Locate every blood parasite and identify its species.
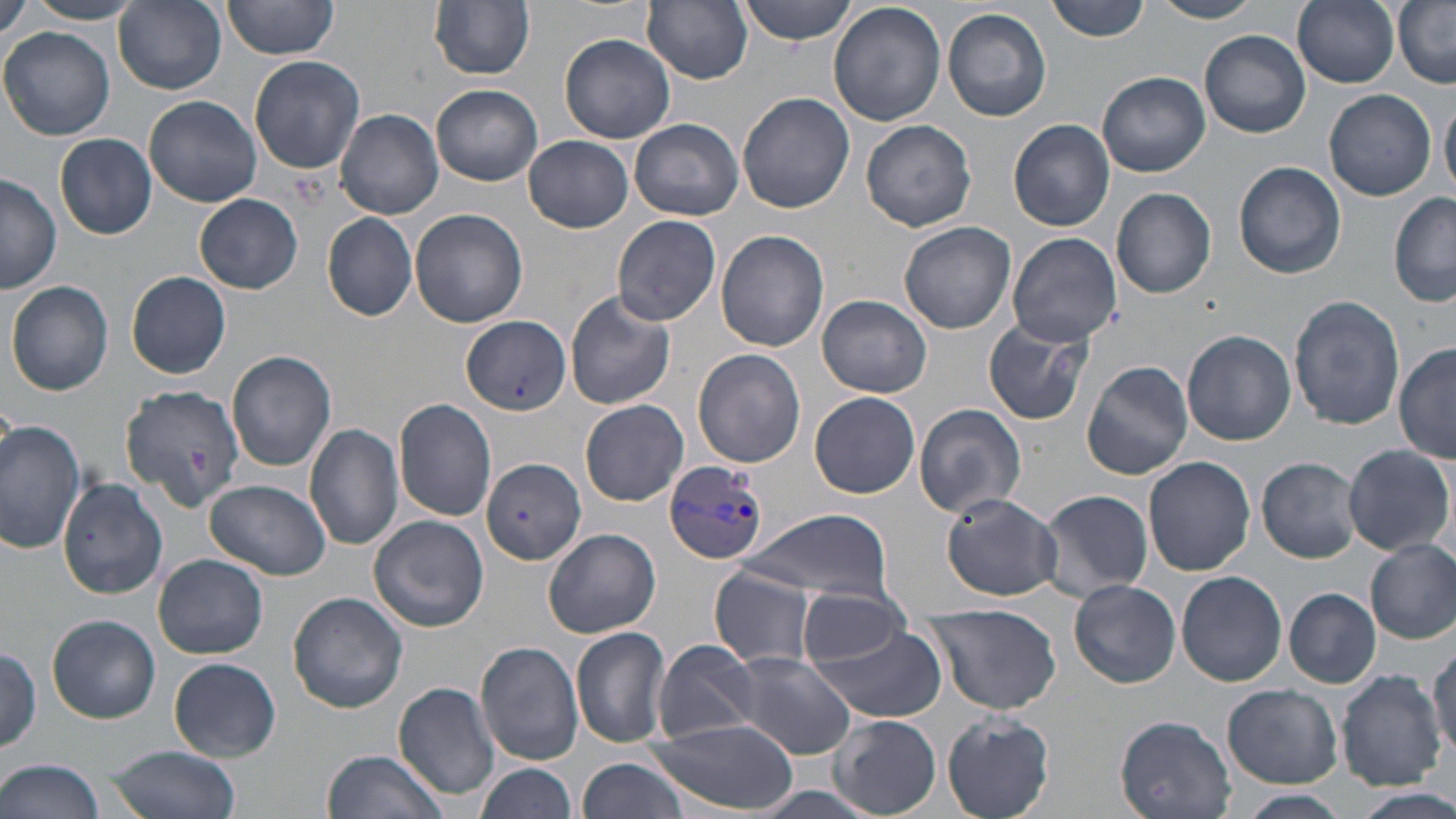

Approximate bounding boxes as (x1,y1)-(x2,y2) corner pairs in pixels.
Plasmodium vivax-infected red blood cells: (661,460)-(769,564).
No Plasmodium falciparum, Plasmodium ovale, Plasmodium malariae, Babesia divergens, or Trypanosoma brucei observed.

Uninfected red blood cell locations: (2,0)-(33,41), (429,0)-(536,80), (643,0)-(753,85), (736,0)-(861,46), (1047,0)-(1152,43), (1150,0)-(1264,23), (1292,0)-(1401,88), (23,1)-(146,24), (114,1)-(227,94), (220,2)-(341,63), (1394,2)-(1456,87), (827,3)-(945,128), (942,8)-(1052,122), (2,27)-(115,140), (1200,30)-(1311,138), (559,33)-(676,144), (249,56)-(365,174), (1099,71)-(1210,177), (431,84)-(543,185), (1323,88)-(1437,201), (737,91)-(854,213), (1440,94)-(1456,200), (144,95)-(262,208), (337,109)-(444,219), (631,118)-(744,221), (1008,119)-(1113,232), (862,120)-(976,233), (54,133)-(157,239), (524,135)-(632,233), (1233,161)-(1347,279), (0,175)-(62,294), (1111,186)-(1218,299), (194,193)-(303,293), (1389,194)-(1455,309), (409,207)-(529,328), (322,214)-(418,322), (612,215)-(723,327), (898,221)-(1016,334), (715,229)-(829,352), (1007,231)-(1120,346), (127,271)-(230,379), (7,279)-(114,396), (564,290)-(677,410), (818,294)-(932,398), (1289,294)-(1405,432), (462,315)-(569,417), (982,316)-(1096,428), (1182,329)-(1296,445), (1394,343)-(1455,464), (692,348)-(806,468), (227,350)-(337,474), (1081,360)-(1194,480), (119,385)-(244,509), (810,392)-(920,498), (393,397)-(498,523), (580,399)-(690,505), (914,404)-(1027,519), (0,419)-(85,557), (305,423)-(404,551), (1343,443)-(1452,556), (1142,456)-(1256,577), (1257,456)-(1363,564), (479,457)-(587,564), (59,473)-(170,603), (205,479)-(330,580), (1039,488)-(1154,601), (942,493)-(1063,600), (742,508)-(895,602), (369,516)-(489,634), (544,528)-(661,639), (1366,538)-(1456,645), (154,553)-(268,659), (710,567)-(819,668), (1176,571)-(1286,686), (1069,579)-(1181,688), (796,588)-(912,665), (1284,588)-(1381,688), (289,591)-(409,714), (922,601)-(1061,715), (48,615)-(160,723), (808,625)-(947,723), (571,626)-(673,749), (476,640)-(584,765), (654,640)-(763,744), (1429,641)-(1456,766), (0,643)-(41,751), (731,654)-(857,759), (168,657)-(282,761), (1334,668)-(1446,791), (394,682)-(500,801), (1223,684)-(1343,787), (941,711)-(1057,818), (831,714)-(941,816), (1117,716)-(1237,819), (645,720)-(800,811), (107,744)-(241,819), (320,749)-(447,819), (579,756)-(690,819), (1,758)-(109,819), (475,762)-(576,819), (742,785)-(885,819), (1357,787)-(1456,819), (1236,791)-(1351,819). Slide-level diagnosis: Plasmodium vivax. May-Grünwald-Giemsa stain. Image is 1456×819 pixels. Thin blood film. 1000x magnification. Optical microscopy. Single field of view.